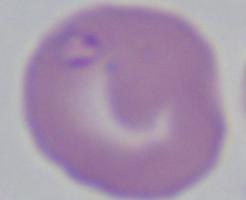

Summary:
  - Magnification: 1000x
  - Modality: photomicrograph
  - Identification: Babesia